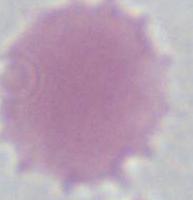

identification = red blood cell
modality = photomicrograph
magnification = 1000x